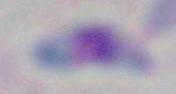

Toxoplasma gondii is shown. 1000x magnification. Photomicrograph.